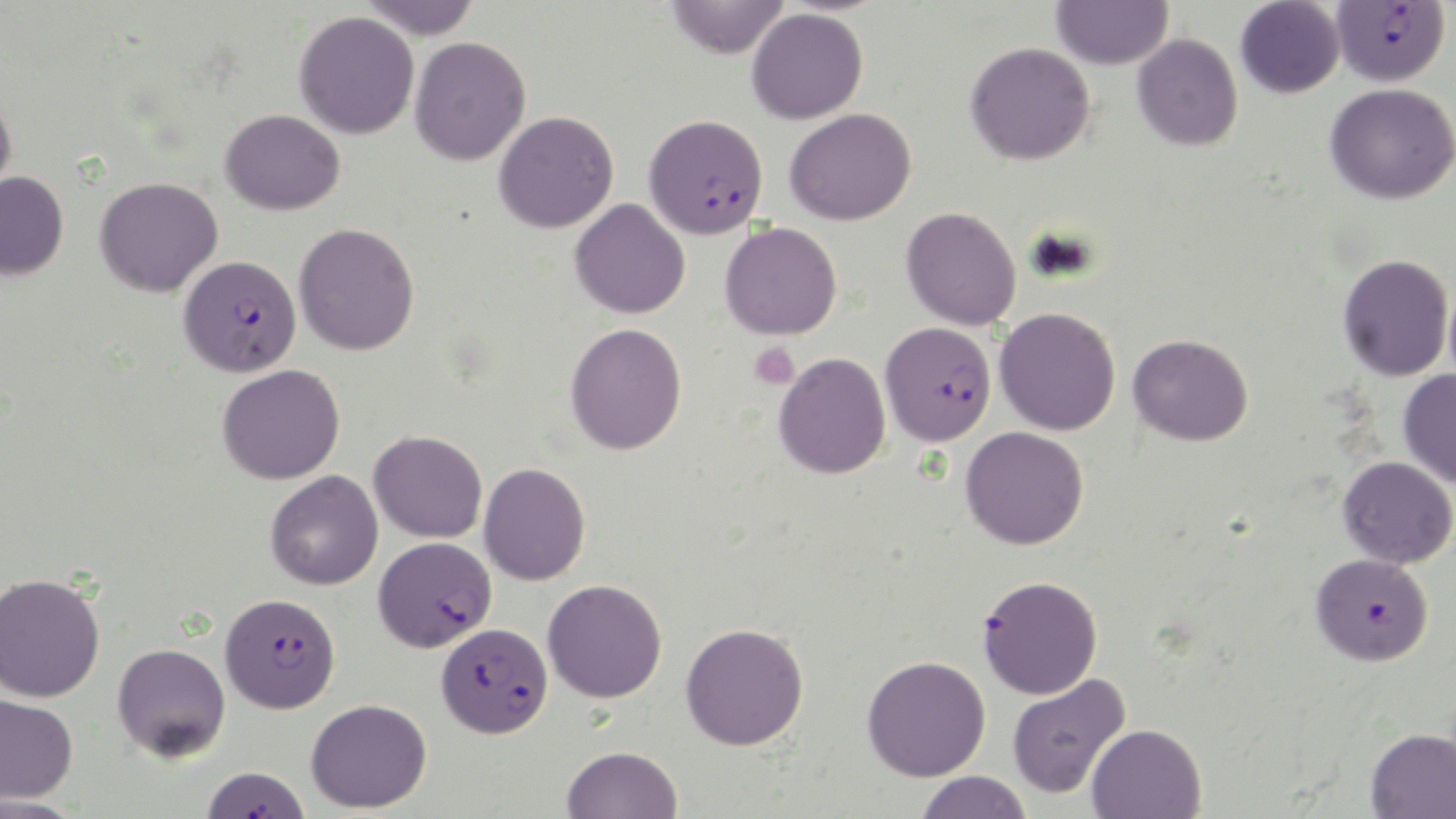

slide-level diagnosis = Plasmodium falciparum
image size = 1456×819 pixels
platelet locations = approximate bounding boxes as [x1, y1, x2, y2] in pixels: [749, 342, 799, 389]
Plasmodium falciparum-infected red blood cell locations (subset) = approximate bounding boxes as [x1, y1, x2, y2] in pixels: [1330, 1, 1450, 87], [643, 114, 768, 239], [179, 254, 302, 376], [879, 322, 997, 446], [374, 536, 497, 653], [1311, 553, 1434, 664], [220, 592, 341, 713], [437, 622, 553, 737], [201, 766, 312, 818]
stain = May-Grünwald-Giemsa
field of view = one of a larger specimen
modality = light microscopy
uninfected red blood cell locations (subset) = approximate bounding boxes as [x1, y1, x2, y2] in pixels: [357, 0, 483, 40], [666, 0, 789, 59], [1051, 0, 1173, 70], [1235, 0, 1344, 99], [746, 8, 868, 125], [294, 11, 419, 139], [1132, 33, 1243, 151], [410, 36, 531, 165], [965, 41, 1095, 165], [1325, 83, 1456, 204], [0, 92, 17, 208], [784, 107, 916, 225], [220, 109, 345, 215], [494, 111, 618, 233], [0, 171, 69, 281], [94, 176, 223, 297], [570, 198, 690, 318], [901, 206, 1021, 330], [294, 222, 419, 355], [720, 222, 842, 340], [1338, 254, 1454, 381], [994, 307, 1121, 436], [565, 322, 687, 455], [1128, 333, 1253, 446], [773, 352, 891, 479], [217, 364, 345, 485], [1398, 369, 1456, 488], [960, 426, 1089, 550], [369, 430, 487, 542], [1338, 456, 1456, 568], [479, 462, 590, 585], [265, 470, 383, 590], [0, 572, 106, 702], [543, 579, 667, 702], [680, 623, 809, 750], [112, 642, 231, 762], [862, 655, 991, 781], [1006, 673, 1130, 799], [0, 693, 79, 804], [306, 698, 432, 813], [1086, 723, 1206, 819], [1365, 728, 1456, 819], [562, 745, 683, 819], [915, 770, 1032, 819], [0, 796, 88, 819]
preparation = thin blood smear
magnification = 1000x